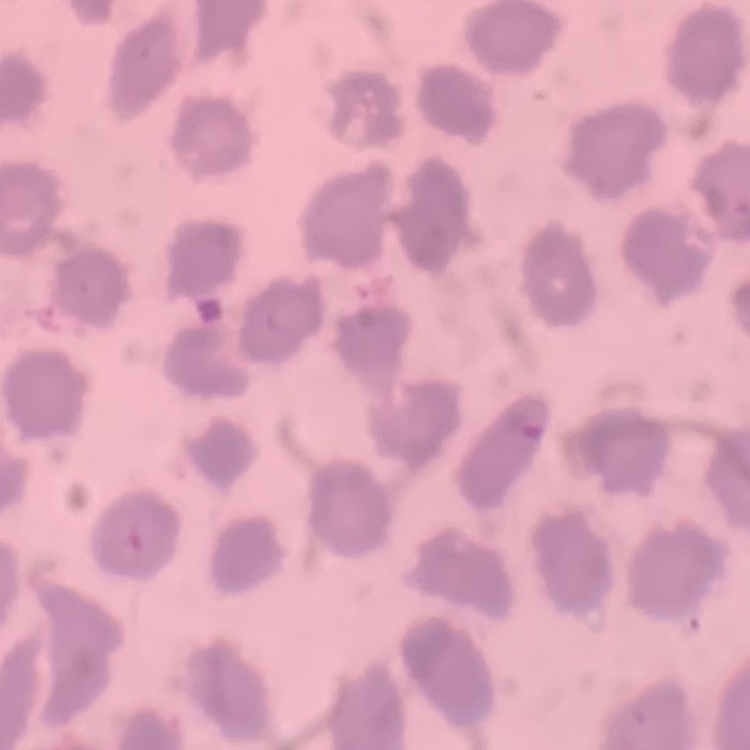
The erythrocytes exhibit no rouleaux formation. Thin blood film. Field's or Giemsa stain. One tile cut from a larger photomicrograph.